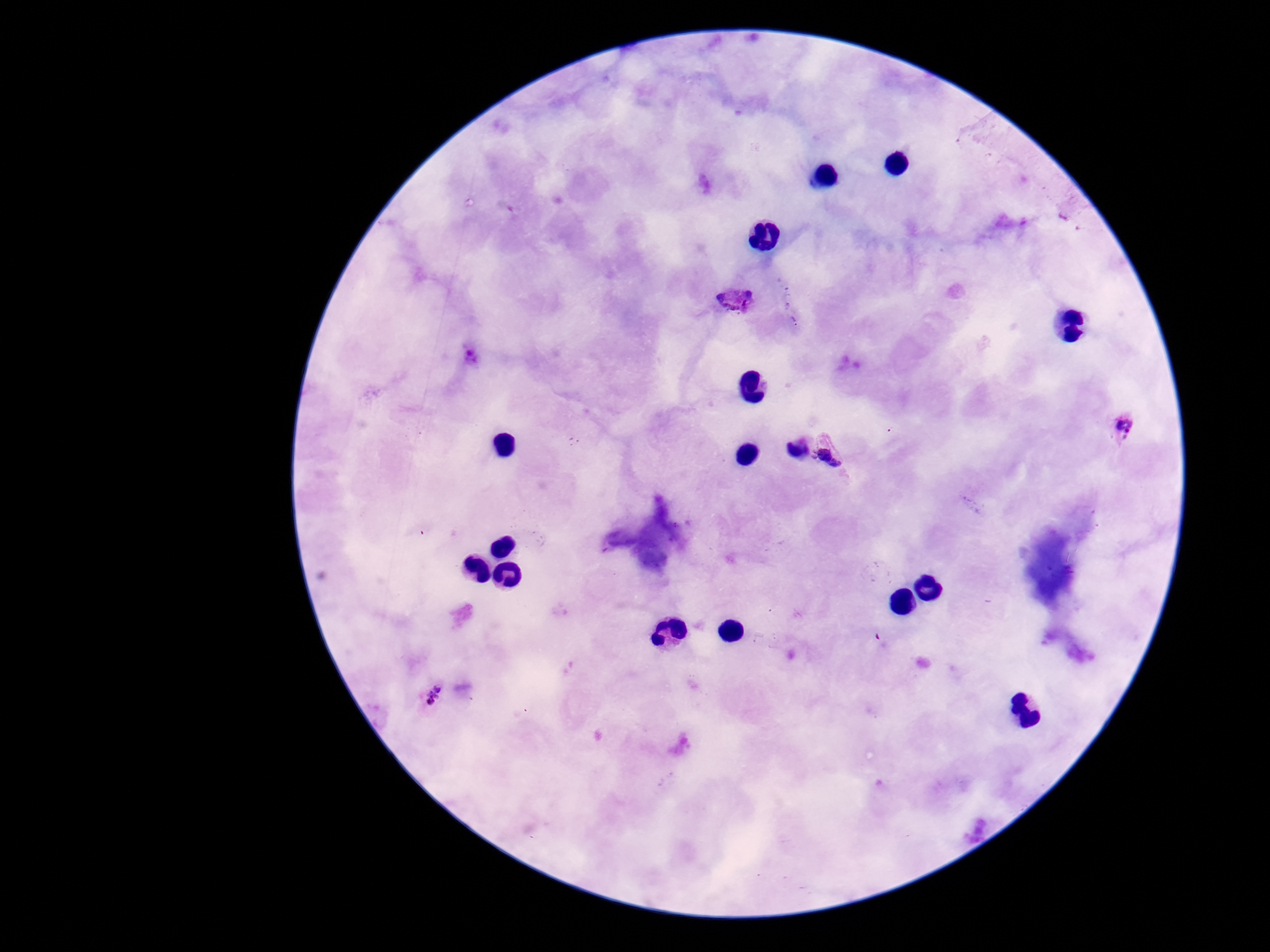

Approximate object centers, in pixels from the top-left corner.
Summary:
  - Plasmodium parasite locations: (x=737, y=302), (x=1127, y=428), (x=792, y=451), (x=839, y=453), (x=431, y=696)
  - Magnification: 100x
  - Field of view: one from this slide
  - Stain: Giemsa
  - Capture: smartphone camera through the microscope eyepiece
  - Patient malaria status: infected
  - Preparation: thick blood smear
  - Image size: 1270×952 pixels